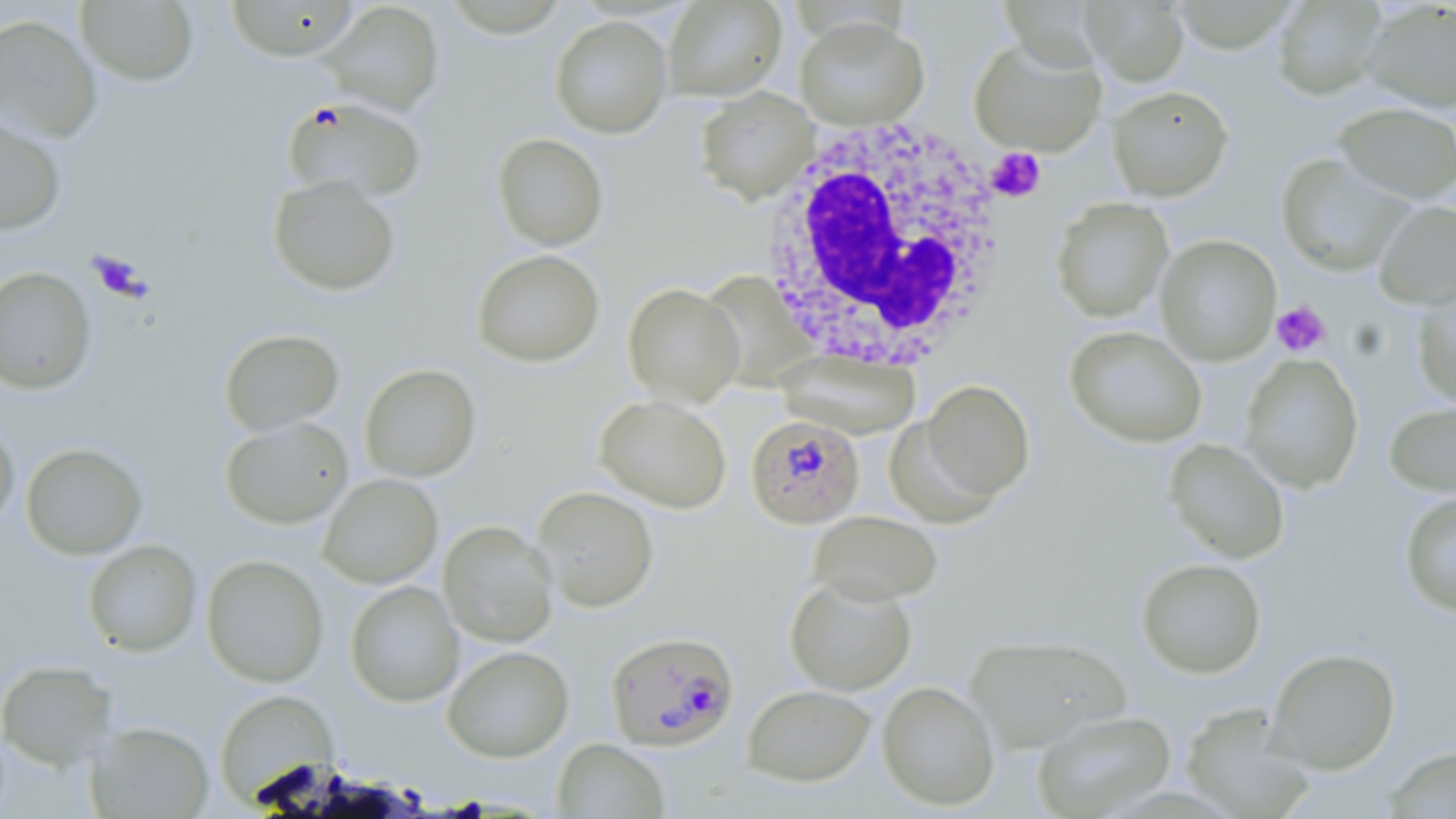

slide-level diagnosis = Plasmodium falciparum
stain = May-Grünwald-Giemsa
modality = optical microscopy
Plasmodium falciparum-infected red blood cell locations = approximate bounding boxes as named x1/y1/x2/y2 corners in pixels: (x1=281, y1=96, x2=428, y2=203), (x1=745, y1=415, x2=865, y2=529), (x1=600, y1=634, x2=734, y2=755)
platelet locations = approximate bounding boxes as named x1/y1/x2/y2 corners in pixels: (x1=987, y1=148, x2=1047, y2=202), (x1=1271, y1=300, x2=1331, y2=357)
field of view = single
uninfected red blood cell locations = approximate bounding boxes as named x1/y1/x2/y2 corners in pixels: (x1=75, y1=0, x2=199, y2=87), (x1=224, y1=0, x2=361, y2=61), (x1=1082, y1=0, x2=1189, y2=86), (x1=1360, y1=0, x2=1456, y2=113), (x1=662, y1=1, x2=787, y2=101), (x1=1270, y1=1, x2=1388, y2=100), (x1=321, y1=2, x2=444, y2=116), (x1=0, y1=13, x2=103, y2=145), (x1=550, y1=15, x2=672, y2=139), (x1=794, y1=15, x2=929, y2=130), (x1=969, y1=36, x2=1106, y2=157), (x1=1107, y1=85, x2=1233, y2=201), (x1=694, y1=87, x2=818, y2=206), (x1=1332, y1=101, x2=1456, y2=205), (x1=0, y1=111, x2=68, y2=237), (x1=492, y1=133, x2=609, y2=250), (x1=1276, y1=153, x2=1412, y2=276), (x1=267, y1=174, x2=401, y2=296), (x1=1050, y1=197, x2=1173, y2=323), (x1=1373, y1=200, x2=1456, y2=310), (x1=1155, y1=234, x2=1281, y2=365), (x1=471, y1=248, x2=605, y2=368), (x1=0, y1=266, x2=96, y2=395), (x1=700, y1=271, x2=819, y2=392), (x1=1411, y1=276, x2=1456, y2=410), (x1=623, y1=283, x2=744, y2=408), (x1=1064, y1=325, x2=1207, y2=448), (x1=218, y1=328, x2=344, y2=436), (x1=775, y1=348, x2=922, y2=440), (x1=1240, y1=354, x2=1363, y2=492), (x1=360, y1=363, x2=482, y2=483), (x1=919, y1=379, x2=1037, y2=501), (x1=594, y1=394, x2=732, y2=513), (x1=1383, y1=400, x2=1456, y2=498), (x1=220, y1=416, x2=354, y2=529), (x1=883, y1=416, x2=1001, y2=528), (x1=0, y1=418, x2=20, y2=538), (x1=1164, y1=438, x2=1291, y2=563), (x1=21, y1=442, x2=147, y2=560), (x1=318, y1=473, x2=442, y2=588), (x1=532, y1=486, x2=659, y2=612), (x1=1399, y1=490, x2=1456, y2=617), (x1=808, y1=510, x2=942, y2=606), (x1=438, y1=520, x2=558, y2=647), (x1=83, y1=539, x2=202, y2=657), (x1=201, y1=555, x2=329, y2=687), (x1=1136, y1=557, x2=1267, y2=678), (x1=784, y1=575, x2=917, y2=696), (x1=345, y1=580, x2=464, y2=707), (x1=963, y1=634, x2=1131, y2=753), (x1=443, y1=646, x2=574, y2=762), (x1=1266, y1=647, x2=1401, y2=774), (x1=0, y1=659, x2=120, y2=771), (x1=877, y1=680, x2=1000, y2=810), (x1=741, y1=684, x2=876, y2=786), (x1=214, y1=689, x2=336, y2=805), (x1=1179, y1=704, x2=1317, y2=818), (x1=1031, y1=709, x2=1177, y2=818), (x1=85, y1=721, x2=215, y2=818), (x1=552, y1=738, x2=670, y2=819), (x1=1381, y1=744, x2=1456, y2=818)
image size = 1456×819 pixels
preparation = thin blood smear
white blood cell locations = approximate bounding boxes as named x1/y1/x2/y2 corners in pixels: (x1=755, y1=117, x2=1010, y2=371)
magnification = 1000x